Report the malaria status of this cell.
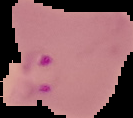
Parasitized.

preparation = thin blood smear
image size = 133×118 pixels
image type = segmented cell region with the area outside set to black